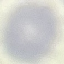
malaria status = uninfected
image type = cell patch, automatically extracted from a larger field of view and resized to 64 × 64 pixels
stain = Giemsa
capture = smartphone camera at the microscope eyepiece
preparation = thin blood smear